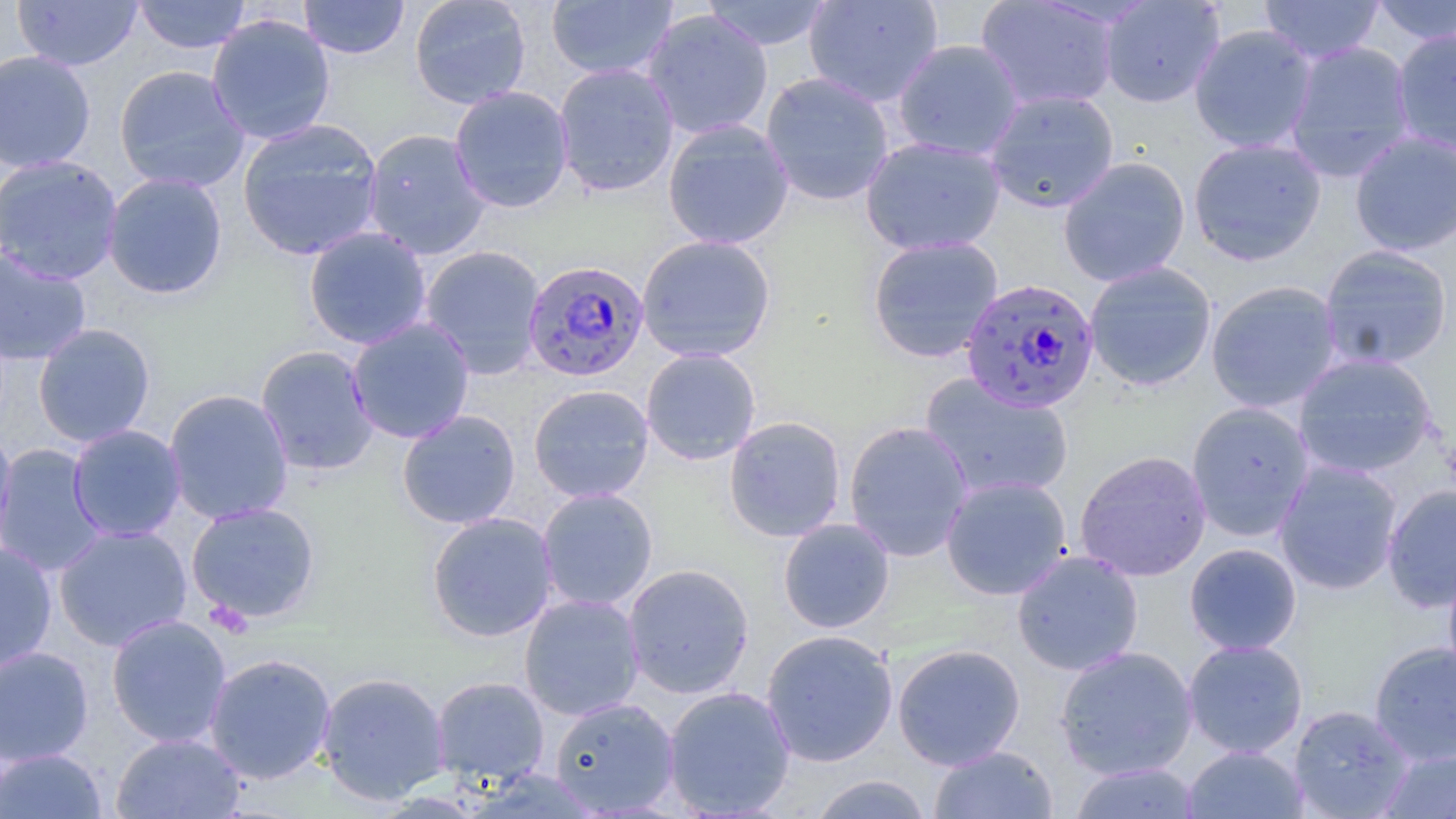

Summary:
  - Coordinate format: approximate bounding boxes as (x1, y1, x2, y2) in pixels
  - Uninfected red blood cell locations: (133, 0, 251, 54), (298, 0, 410, 59), (409, 0, 531, 109), (545, 0, 679, 81), (699, 0, 834, 51), (804, 0, 943, 108), (1098, 0, 1225, 108), (1258, 0, 1385, 65), (12, 1, 143, 71), (975, 1, 1121, 112), (1370, 1, 1456, 46), (640, 9, 774, 140), (206, 14, 336, 145), (1189, 24, 1318, 153), (1391, 28, 1456, 157), (892, 39, 1025, 161), (1283, 40, 1416, 182), (0, 49, 96, 173), (553, 63, 680, 198), (113, 64, 250, 193), (760, 71, 895, 207), (449, 85, 574, 213), (984, 89, 1119, 213), (236, 118, 384, 261), (662, 119, 795, 251), (362, 128, 491, 260), (1350, 130, 1456, 256), (860, 136, 1006, 256), (1187, 137, 1327, 266), (0, 154, 124, 286), (1058, 157, 1190, 287), (102, 172, 229, 300), (303, 226, 432, 350), (637, 235, 776, 363), (867, 235, 1004, 363), (419, 244, 546, 379), (1319, 244, 1454, 370), (0, 248, 93, 366), (1084, 261, 1217, 391), (1205, 281, 1342, 413), (346, 318, 475, 444), (32, 323, 156, 447), (256, 345, 379, 476), (640, 348, 761, 466), (1293, 352, 1439, 479), (919, 372, 1075, 502), (528, 384, 654, 504), (163, 388, 294, 525), (1186, 400, 1315, 541), (397, 409, 521, 529), (723, 415, 847, 542), (843, 420, 975, 562), (67, 424, 187, 543), (0, 425, 17, 562), (0, 444, 108, 576), (1074, 449, 1212, 582), (1274, 459, 1404, 595), (940, 475, 1073, 600), (1382, 484, 1456, 613), (536, 487, 658, 612), (185, 501, 322, 624), (425, 512, 558, 642), (778, 518, 895, 633), (54, 524, 193, 652), (1184, 542, 1302, 656), (0, 543, 58, 672), (1011, 549, 1144, 676), (1443, 556, 1456, 685), (622, 563, 755, 699), (519, 593, 645, 721), (105, 614, 233, 748), (760, 629, 898, 767), (1182, 639, 1308, 758), (1369, 640, 1456, 767), (892, 643, 1025, 770), (0, 645, 94, 767), (1054, 646, 1198, 780), (203, 652, 337, 784), (316, 670, 450, 805), (430, 675, 549, 787), (662, 685, 796, 818), (549, 697, 680, 816), (1288, 705, 1414, 818), (111, 731, 246, 818), (929, 744, 1058, 818), (1181, 745, 1310, 818), (1377, 747, 1456, 818), (0, 748, 108, 818), (1068, 761, 1202, 818), (806, 774, 934, 819)
  - Plasmodium falciparum-infected red blood cell locations: (523, 260, 649, 383), (960, 278, 1100, 414)
  - Slide-level diagnosis: Plasmodium falciparum
  - Modality: optical microscopy
  - Image size: 1456×819 pixels
  - Stain: May-Grünwald-Giemsa
  - Preparation: thin blood smear
  - Field of view: single
  - Magnification: 1000x